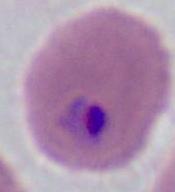
identification: Plasmodium
modality: photomicrograph
magnification: 400x or 1000x